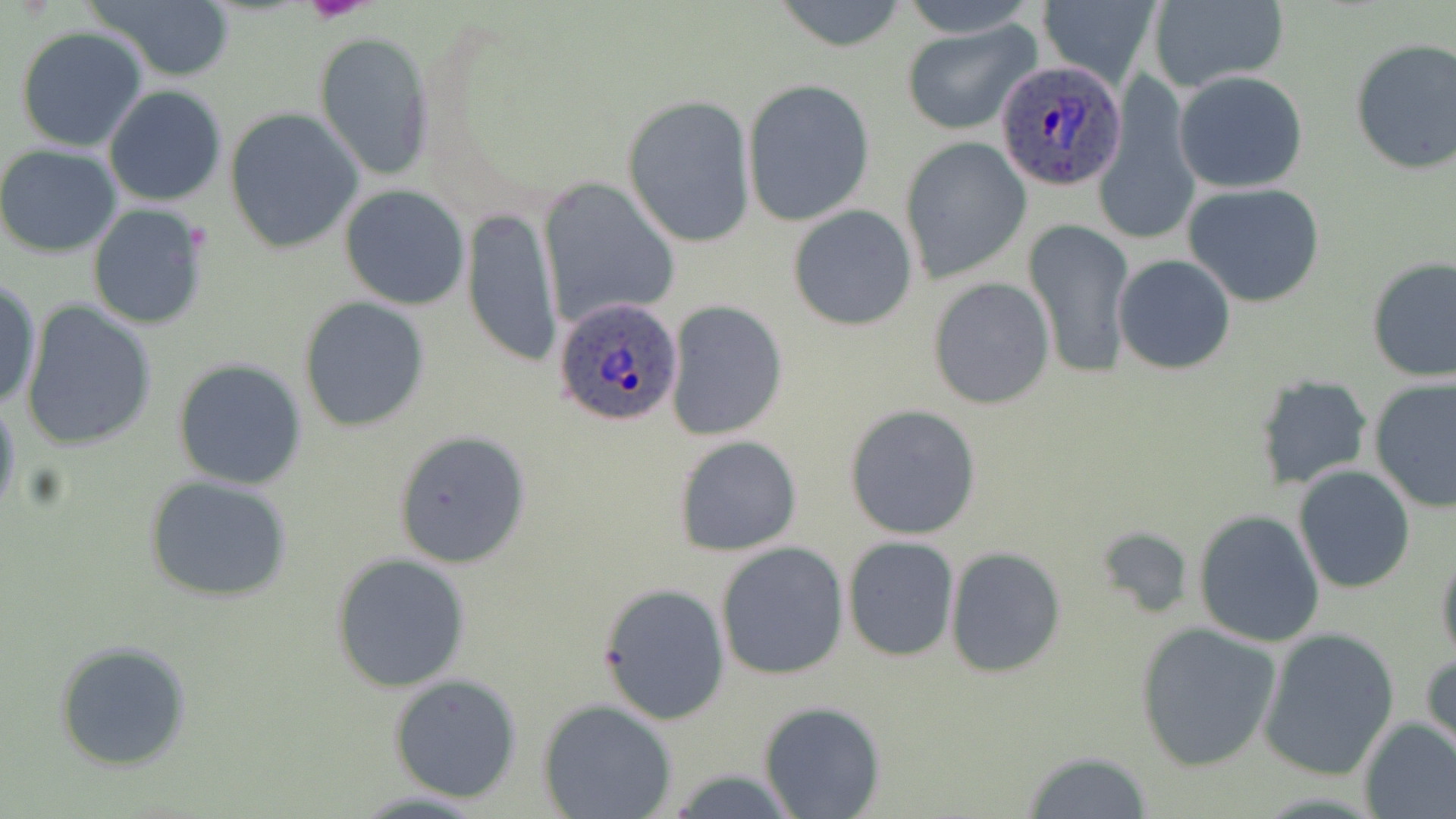

{
  "slide_level_diagnosis": "Plasmodium ovale",
  "magnification": "1000x",
  "stain": "May-Grünwald-Giemsa",
  "platelet_locations": "approximate bounding boxes as (x1,y1)-(x2,y2) corner pairs in pixels: (306,0)-(370,23)",
  "image_size": "1456×819 pixels",
  "modality": "light microscopy",
  "field_of_view": "one of a larger specimen",
  "uninfected_red_blood_cell_locations": "approximate bounding boxes as (x1,y1)-(x2,y2) corner pairs in pixels: (87,0)-(236,81), (773,0)-(911,52), (898,0)-(1039,36), (1039,0)-(1159,90), (1147,1)-(1289,93), (901,21)-(1041,136), (16,25)-(147,152), (315,30)-(434,181), (1348,39)-(1456,178), (1173,70)-(1309,193), (742,79)-(875,225), (1094,79)-(1197,246), (104,85)-(228,207), (623,94)-(755,247), (225,109)-(363,254), (902,137)-(1029,281), (0,144)-(123,257), (538,179)-(678,326), (1183,183)-(1326,308), (339,185)-(471,310), (86,203)-(210,331), (788,204)-(918,331), (463,205)-(561,369), (1026,218)-(1133,383), (1113,255)-(1237,373), (1366,256)-(1456,383), (927,278)-(1053,412), (1,279)-(41,410), (298,297)-(431,432), (665,301)-(788,440), (21,302)-(157,452), (172,357)-(307,490), (1256,375)-(1370,490), (1368,378)-(1456,516), (0,394)-(21,525), (844,404)-(983,540), (395,429)-(530,569), (674,435)-(801,557), (1293,466)-(1416,593), (143,475)-(295,602), (1194,510)-(1326,648), (1095,528)-(1197,619), (842,537)-(959,661), (716,542)-(849,681), (1435,544)-(1456,668), (945,547)-(1067,678), (330,553)-(474,693), (596,582)-(730,725), (1133,622)-(1282,772), (1258,627)-(1399,782), (54,639)-(193,771), (1421,651)-(1455,758), (388,673)-(522,802), (538,700)-(677,818), (758,701)-(886,818), (1358,718)-(1456,819), (1021,750)-(1154,817)",
  "plasmodium_ovale_infected_red_blood_cell_locations": "approximate bounding boxes as (x1,y1)-(x2,y2) corner pairs in pixels: (995,56)-(1129,192), (555,295)-(686,430)",
  "preparation": "thin blood smear"
}